Assess for Plasmodium parasites.
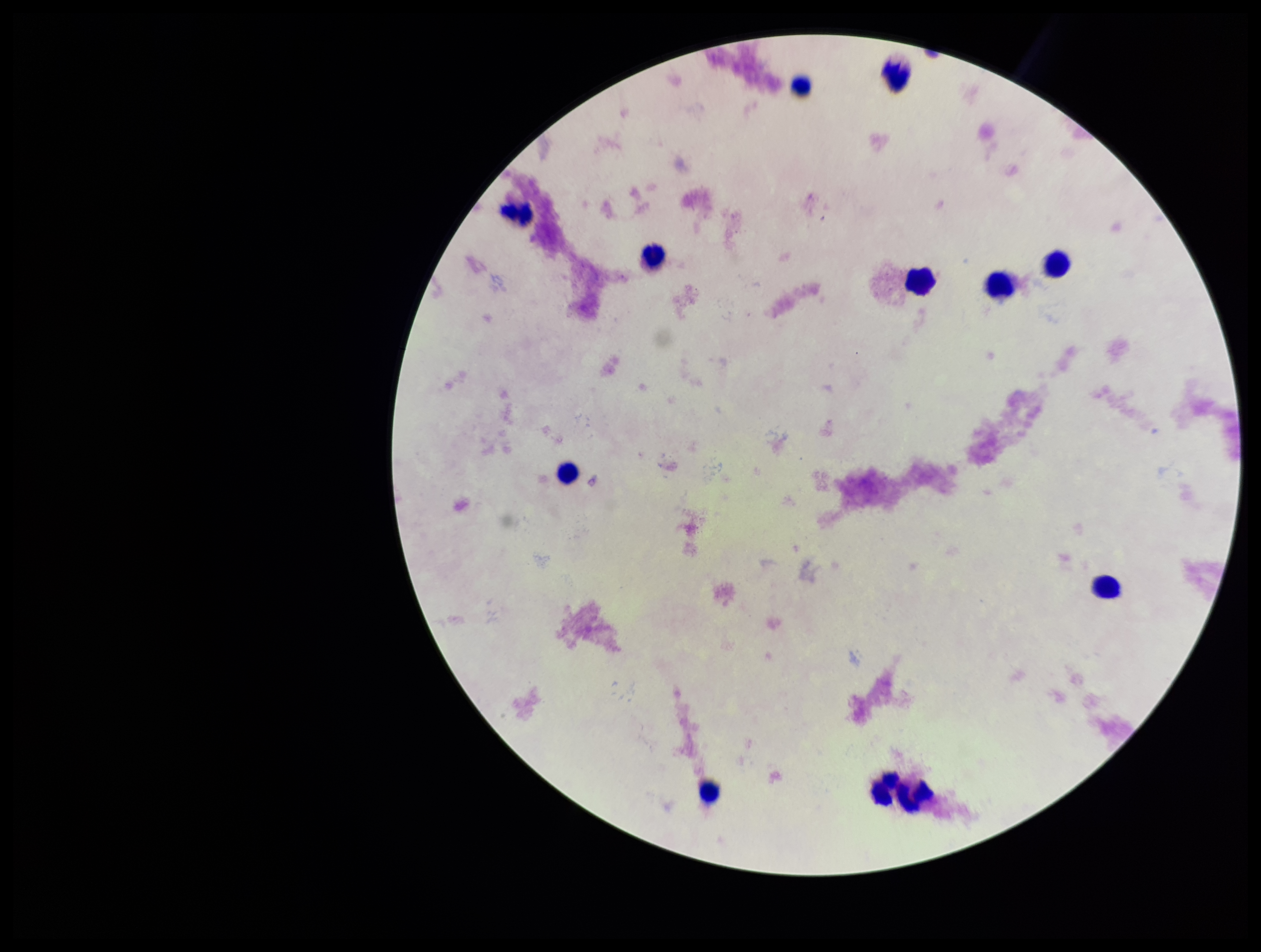
None seen.

Summary:
  - Patient malaria status: negative
  - Image size: 1261×952 pixels
  - Parasite count: 0
  - Preparation: thick smear
  - Field of view: single
  - Stain: Giemsa
  - Capture: smartphone photograph through the microscope eyepiece
  - Leukocyte count: 11